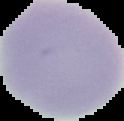

The area outside the segmented cell region is set to black. Image is 124×121 pixels. Result: negative for Plasmodium parasites. From a thin blood film.